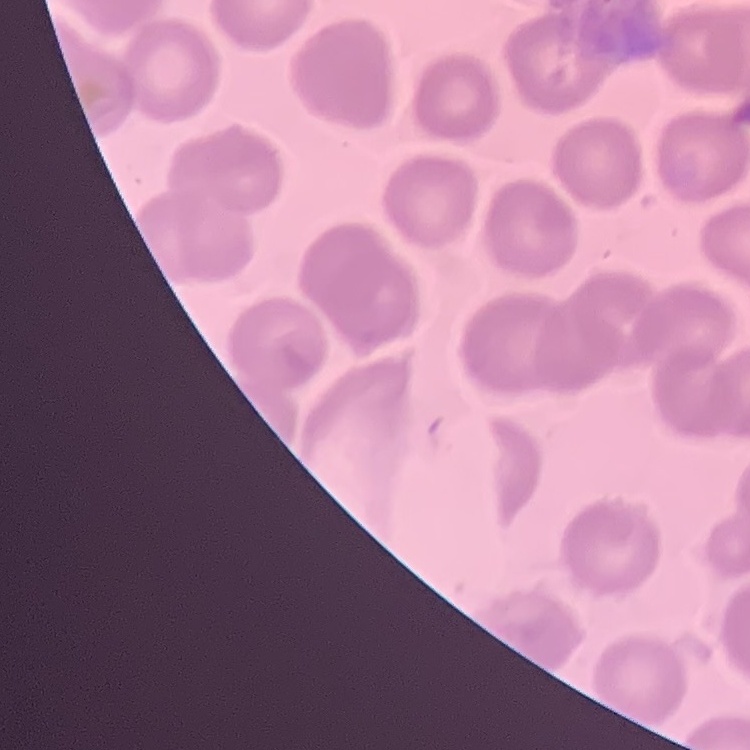
The red blood cells show no rouleaux formation. Thin blood film. Square crop of a larger photomicrograph. Stained with either Field's or Giemsa.